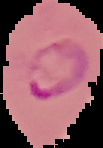
Summary:
  - Malaria status: parasitized
  - Image type: segmented cell region with the area outside set to black
  - Preparation: thin blood smear
  - Image size: 103×148 pixels